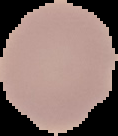 Result: no malaria parasites detected. Image is 118×136 pixels. From a thin blood smear. Segmented cell region on a black background.